Identify the blood parasite species.
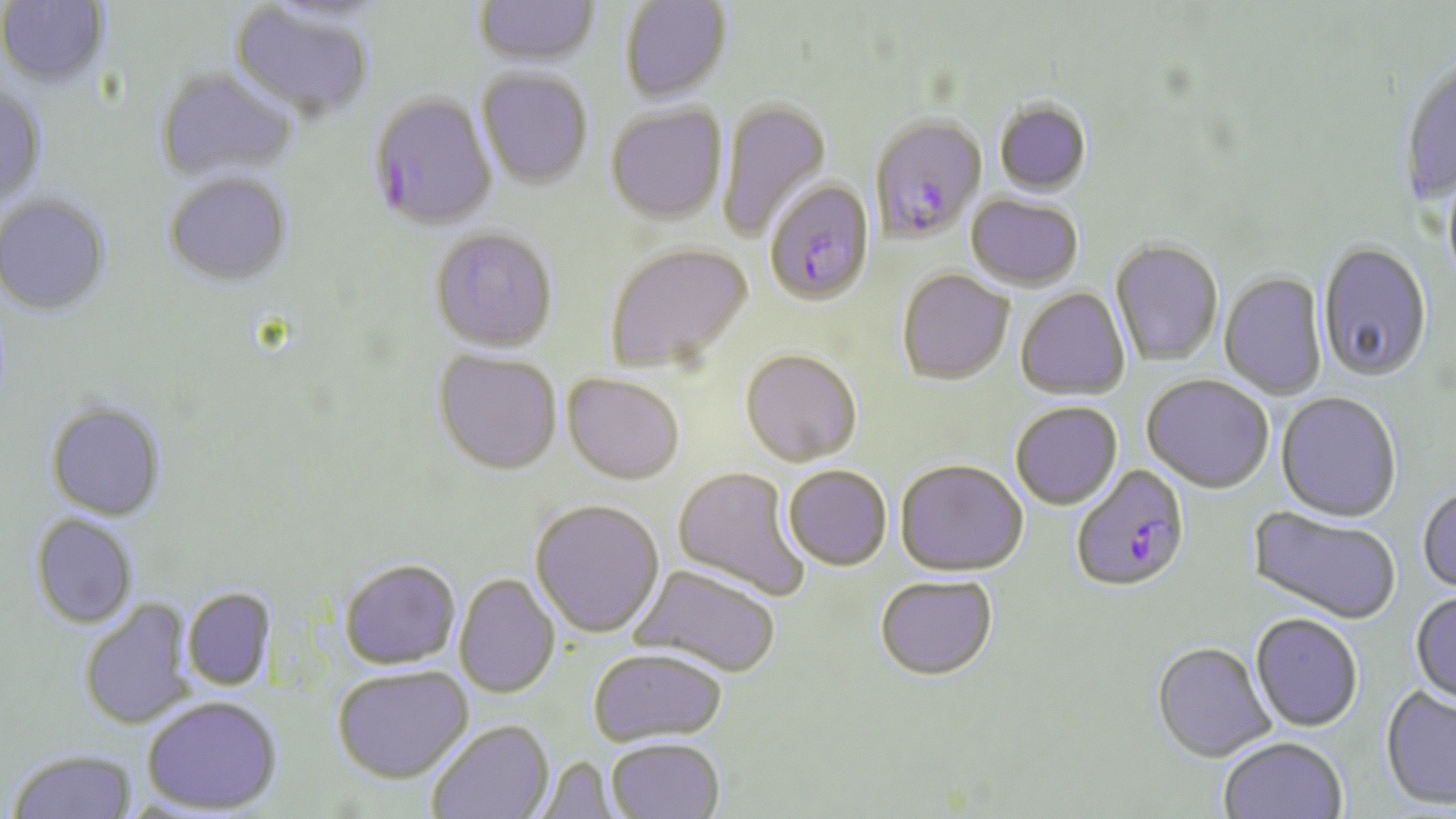
Plasmodium falciparum.

Approximate bounding boxes as (x1, y1, x2, y2) in pixels. Uninfected red blood cell locations: (472, 0, 602, 70), (619, 0, 733, 104), (0, 1, 112, 90), (227, 3, 376, 122), (1399, 58, 1456, 204), (154, 66, 298, 184), (476, 69, 593, 189), (0, 84, 48, 208), (715, 97, 833, 242), (993, 99, 1093, 196), (604, 104, 728, 225), (1442, 169, 1456, 293), (163, 171, 294, 287), (965, 194, 1083, 291), (0, 195, 112, 317), (429, 228, 558, 353), (1109, 240, 1224, 366), (1317, 242, 1433, 383), (604, 243, 753, 373), (896, 268, 1014, 385), (1219, 272, 1328, 400), (1015, 287, 1130, 400), (741, 348, 863, 466), (433, 349, 562, 475), (562, 373, 684, 484), (1141, 374, 1274, 493), (1276, 392, 1403, 524), (45, 401, 167, 521), (1010, 401, 1123, 510), (895, 459, 1028, 576), (782, 464, 893, 571), (672, 466, 811, 601), (1416, 485, 1456, 595), (530, 498, 665, 637), (1247, 506, 1402, 626), (29, 513, 139, 629), (339, 558, 462, 669), (629, 564, 782, 677), (454, 573, 561, 698), (874, 575, 998, 680), (182, 587, 277, 690), (1410, 591, 1456, 706), (78, 599, 196, 730), (1250, 613, 1364, 732), (1152, 641, 1276, 761), (587, 647, 728, 746), (332, 666, 473, 783), (1380, 685, 1456, 810), (142, 695, 283, 814), (426, 719, 555, 819), (605, 737, 725, 819), (1217, 737, 1348, 817), (7, 747, 138, 818), (532, 756, 622, 818). Plasmodium falciparum-infected red blood cell locations: (367, 94, 497, 231), (868, 114, 987, 243), (763, 178, 875, 305), (1070, 465, 1191, 593). Thin blood film. Image is 1456×819 pixels. Light microscopy. Single field of view. May-Grünwald-Giemsa stain. Captured at 1000x magnification.